Assess this cell for malaria.
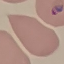
It is uninfected.

stain = Giemsa
image type = automatically extracted cell patch, resized to 64 × 64 pixels
preparation = thin smear
capture = smartphone through the microscope eyepiece